Locate every Plasmodium malariae-infected red blood cell.
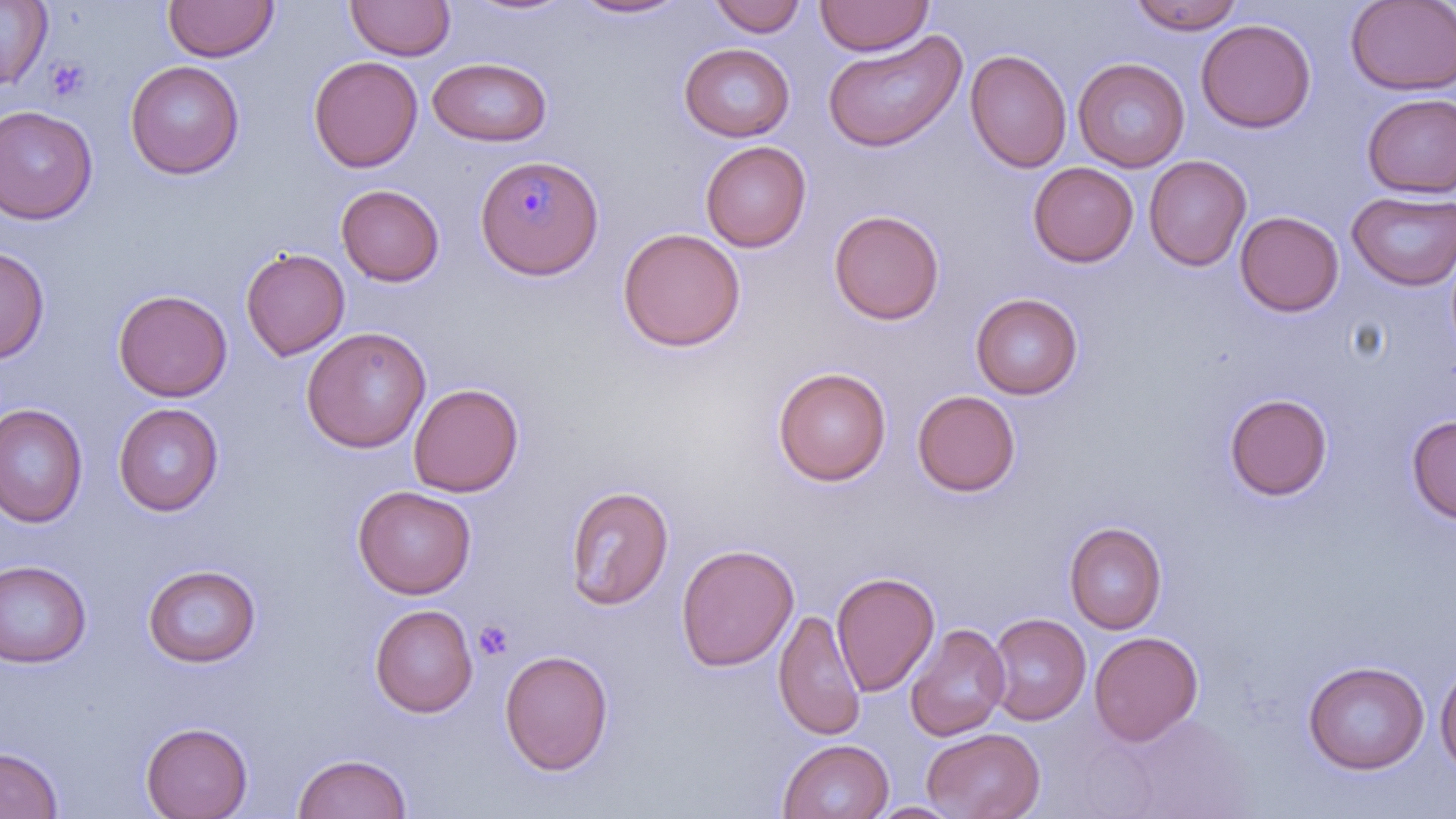

Approximate bounding boxes as named x1/y1/x2/y2 corners in pixels.
Plasmodium malariae-infected red blood cells: (x1=475, y1=154, x2=605, y2=280).

Platelet locations: (x1=45, y1=57, x2=91, y2=103), (x1=473, y1=620, x2=514, y2=660). Uninfected red blood cell locations: (x1=163, y1=0, x2=279, y2=62), (x1=345, y1=0, x2=456, y2=61), (x1=708, y1=0, x2=807, y2=37), (x1=815, y1=0, x2=934, y2=56), (x1=1127, y1=0, x2=1247, y2=35), (x1=0, y1=1, x2=51, y2=88), (x1=463, y1=1, x2=576, y2=17), (x1=570, y1=1, x2=687, y2=19), (x1=1344, y1=1, x2=1456, y2=95), (x1=1196, y1=18, x2=1316, y2=133), (x1=822, y1=29, x2=967, y2=153), (x1=679, y1=43, x2=796, y2=142), (x1=965, y1=49, x2=1071, y2=173), (x1=308, y1=55, x2=423, y2=172), (x1=428, y1=57, x2=552, y2=147), (x1=1073, y1=57, x2=1190, y2=172), (x1=125, y1=60, x2=244, y2=179), (x1=1361, y1=93, x2=1456, y2=198), (x1=0, y1=105, x2=97, y2=224), (x1=700, y1=141, x2=811, y2=252), (x1=1144, y1=155, x2=1251, y2=271), (x1=1028, y1=162, x2=1138, y2=267), (x1=336, y1=184, x2=444, y2=286), (x1=1347, y1=190, x2=1456, y2=290), (x1=828, y1=209, x2=945, y2=324), (x1=1235, y1=211, x2=1344, y2=317), (x1=617, y1=228, x2=746, y2=352), (x1=0, y1=245, x2=49, y2=364), (x1=240, y1=246, x2=350, y2=361), (x1=112, y1=289, x2=232, y2=402), (x1=970, y1=293, x2=1083, y2=400), (x1=301, y1=326, x2=431, y2=453), (x1=772, y1=367, x2=891, y2=486), (x1=408, y1=383, x2=524, y2=497), (x1=912, y1=390, x2=1021, y2=497), (x1=1224, y1=393, x2=1332, y2=500), (x1=113, y1=402, x2=224, y2=516), (x1=0, y1=403, x2=88, y2=527), (x1=1406, y1=415, x2=1456, y2=524), (x1=563, y1=484, x2=674, y2=611), (x1=352, y1=485, x2=477, y2=599), (x1=1064, y1=521, x2=1167, y2=634), (x1=676, y1=543, x2=798, y2=672), (x1=0, y1=559, x2=91, y2=668), (x1=143, y1=563, x2=261, y2=667), (x1=831, y1=570, x2=940, y2=697), (x1=370, y1=604, x2=478, y2=718), (x1=773, y1=608, x2=866, y2=742), (x1=987, y1=613, x2=1091, y2=725), (x1=904, y1=623, x2=1010, y2=742), (x1=1089, y1=631, x2=1203, y2=747), (x1=499, y1=649, x2=614, y2=775), (x1=1435, y1=659, x2=1456, y2=776), (x1=1302, y1=660, x2=1430, y2=774), (x1=141, y1=721, x2=252, y2=818), (x1=922, y1=727, x2=1045, y2=819), (x1=778, y1=738, x2=894, y2=819), (x1=0, y1=747, x2=63, y2=819), (x1=292, y1=752, x2=411, y2=819), (x1=868, y1=801, x2=965, y2=818). Slide-level diagnosis: Plasmodium malariae. Captured at 1000x magnification. Thin blood smear. One field of a larger specimen. Light microscopy. May-Grünwald-Giemsa-stained preparation. Image is 1456×819 pixels.